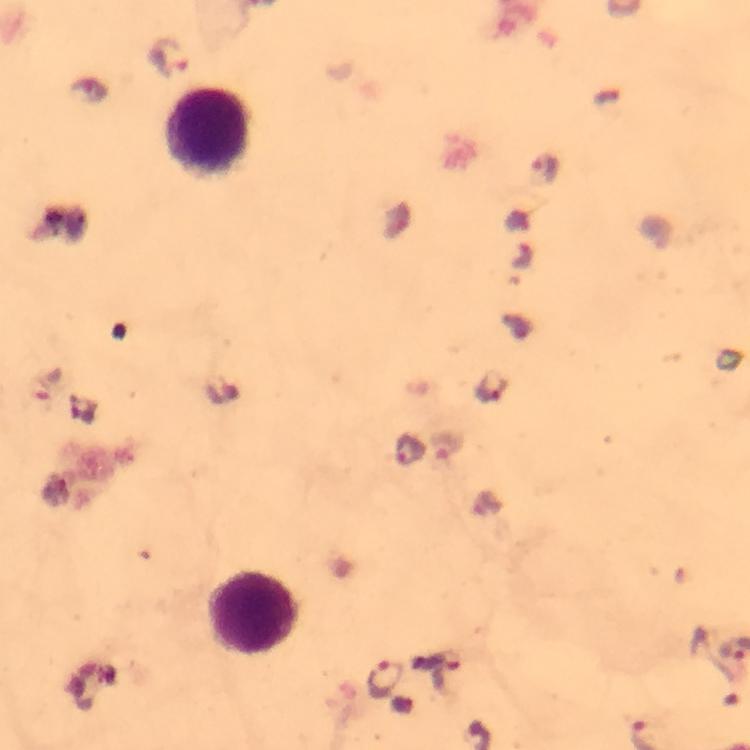
Approximate centers as {x, y} in pixels.
Summary:
  - Malaria parasite locations: {171, 56}, {546, 166}, {493, 386}, {445, 446}, {407, 450}, {385, 678}
  - Leukocyte locations: {206, 132}, {254, 612}
  - Preparation: thick smear
  - Image size: 750×750 pixels
  - Context: from a malaria diagnostic workup
  - Immersion oil: applied
  - Stain: Giemsa
  - Magnification: 100x
  - Capture: smartphone camera through the microscope
  - Cropped from: a single field of view